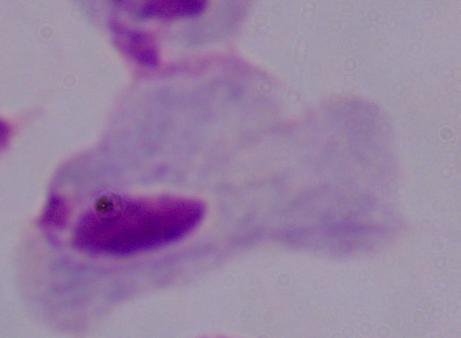

A trichomonad is shown. Micrograph. Captured at 1000x magnification.